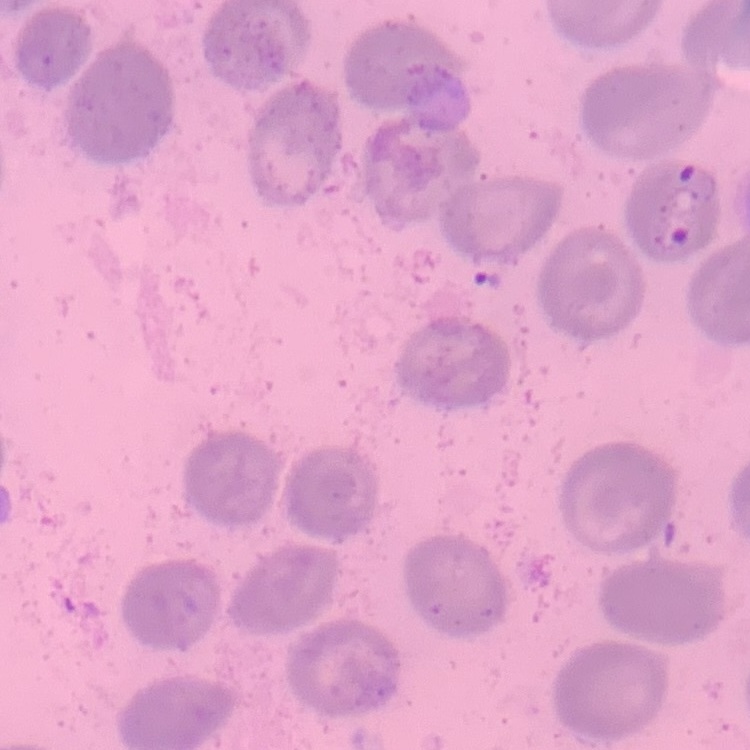

The erythrocytes exhibit no rouleaux formation. Stained with either Field's or Giemsa. Thin blood film. One tile cut from a larger photomicrograph.